Identify the blood parasite species.
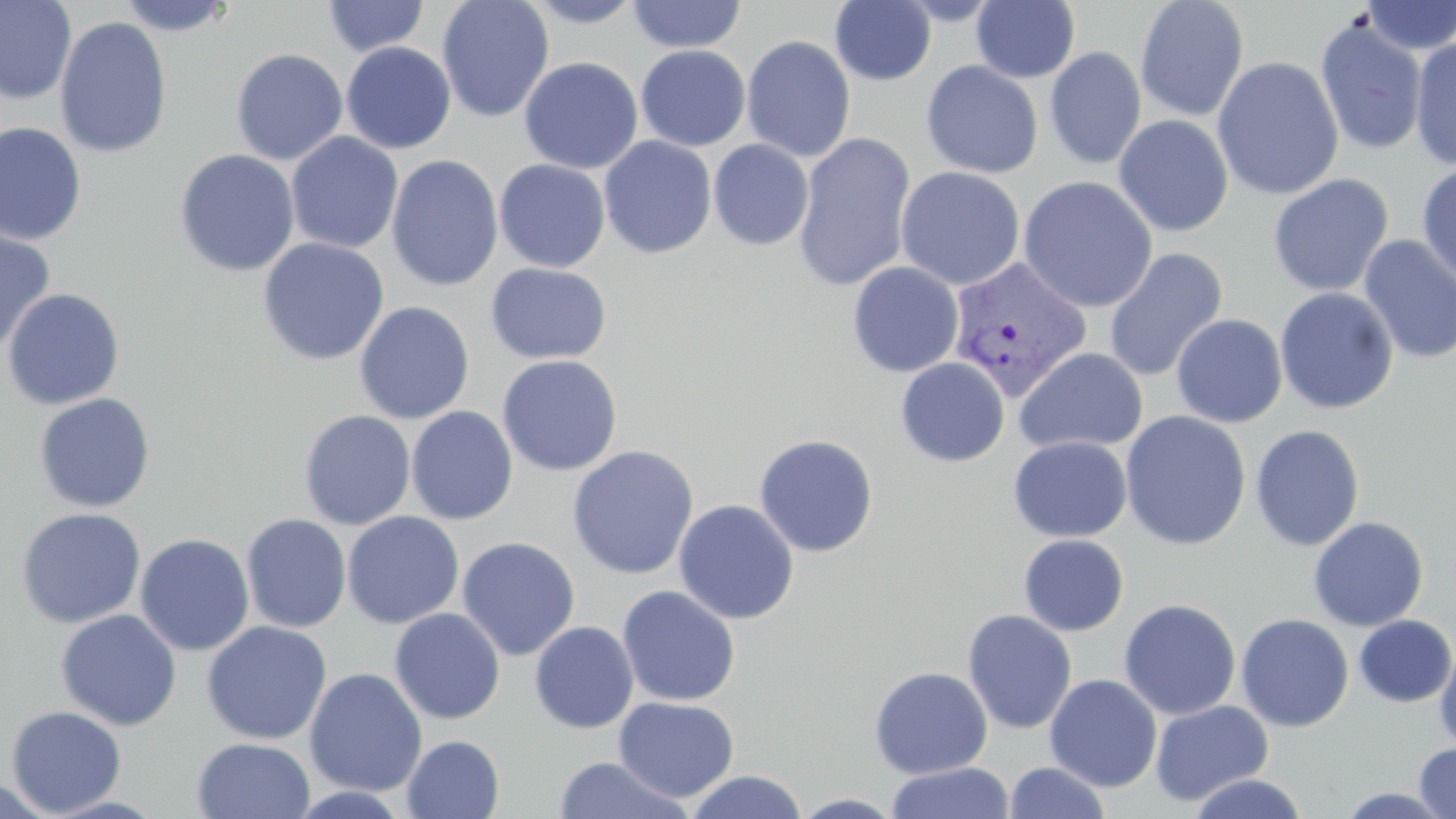
Plasmodium vivax.

Summary:
  - Coordinate format: approximate bounding boxes as (x1, y1, x2, y2) in pixels
  - Uninfected red blood cell locations: (0, 0, 77, 104), (115, 0, 238, 36), (322, 0, 429, 57), (436, 0, 555, 123), (520, 0, 648, 27), (1135, 0, 1250, 122), (1358, 0, 1456, 55), (626, 1, 747, 53), (830, 1, 937, 86), (970, 1, 1080, 83), (55, 15, 172, 158), (1315, 16, 1428, 156), (741, 35, 856, 162), (1409, 37, 1456, 171), (341, 42, 456, 154), (635, 45, 751, 151), (1045, 47, 1147, 170), (230, 48, 348, 165), (1211, 56, 1344, 200), (519, 57, 643, 174), (505, 58, 629, 274), (922, 60, 1044, 178), (1113, 115, 1233, 237), (0, 122, 87, 245), (286, 131, 404, 254), (793, 131, 917, 293), (599, 136, 717, 259), (708, 140, 814, 251), (174, 149, 300, 277), (386, 154, 503, 292), (494, 159, 610, 272), (1416, 160, 1456, 290), (895, 166, 1026, 290), (1267, 174, 1394, 297), (1018, 176, 1158, 312), (0, 224, 57, 354), (1358, 235, 1456, 363), (257, 237, 390, 365), (1103, 248, 1228, 382), (847, 261, 964, 377), (485, 262, 611, 364), (1274, 287, 1399, 414), (2, 288, 125, 411), (354, 300, 475, 423), (1171, 313, 1288, 428), (1013, 347, 1148, 455), (497, 354, 623, 476), (895, 358, 1010, 467), (34, 393, 156, 512), (406, 406, 518, 525), (299, 410, 416, 530), (1120, 410, 1251, 549), (1250, 424, 1365, 551), (754, 434, 879, 557), (1008, 436, 1132, 542), (566, 445, 700, 580), (673, 499, 800, 625), (16, 507, 146, 628), (342, 511, 464, 629), (240, 513, 351, 633), (1308, 516, 1429, 631), (135, 533, 255, 655), (1018, 534, 1129, 636), (457, 536, 580, 661), (617, 586, 741, 706), (1118, 599, 1241, 720), (389, 608, 506, 724), (55, 609, 181, 731), (961, 609, 1077, 735), (1235, 613, 1355, 732), (1354, 615, 1456, 707), (202, 621, 332, 744), (529, 621, 639, 734), (1435, 644, 1456, 754), (869, 666, 993, 778), (304, 667, 428, 797), (1044, 674, 1163, 791), (613, 697, 739, 802), (1150, 700, 1273, 806), (5, 706, 127, 816), (401, 735, 505, 818), (193, 737, 316, 819), (1414, 741, 1456, 819), (551, 755, 696, 818), (1003, 761, 1111, 819), (886, 762, 1015, 819), (684, 770, 809, 818), (1185, 772, 1310, 818), (0, 775, 57, 818), (791, 793, 907, 818)
  - Plasmodium vivax-infected red blood cell locations: (947, 255, 1092, 401)
  - Field of view: single
  - Modality: optical microscopy
  - Image size: 1456×819 pixels
  - Magnification: 1000x
  - Stain: May-Grünwald-Giemsa
  - Preparation: thin blood film